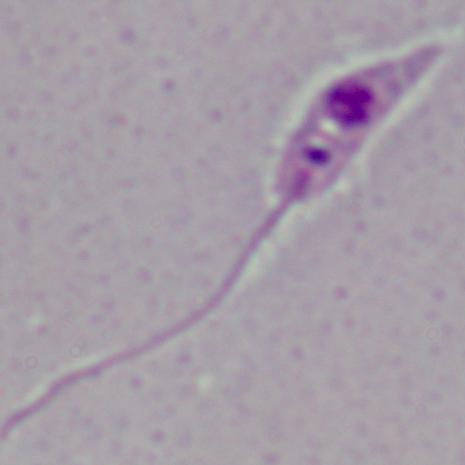

{
  "modality": "photomicrograph",
  "magnification": "1000x",
  "identification": "Leishmania"
}